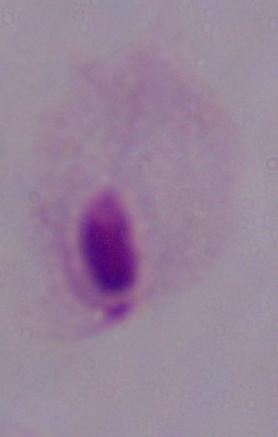

Summary:
  - Modality: micrograph
  - Identification: trichomonad
  - Magnification: 1000x